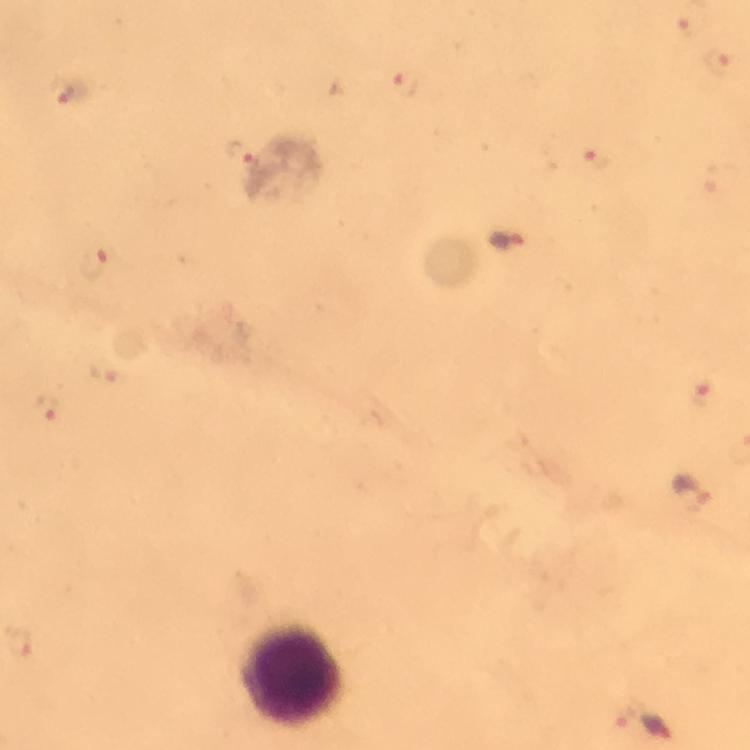
Approximate centers as (x, y) in pixels. Leukocyte locations: (293, 674). Malaria parasite locations: (405, 83), (71, 92), (239, 152), (595, 162), (504, 242), (96, 264), (704, 395), (49, 407), (693, 494), (19, 644), (643, 724). Immersion oil was used. Image is 750×750 pixels. From a malaria diagnostic workup. Smartphone photograph taken through a microscope. A crop from one field of view. Giemsa stain. At 100x magnification. Thick smear.